Outline each uninfected red blood cell.
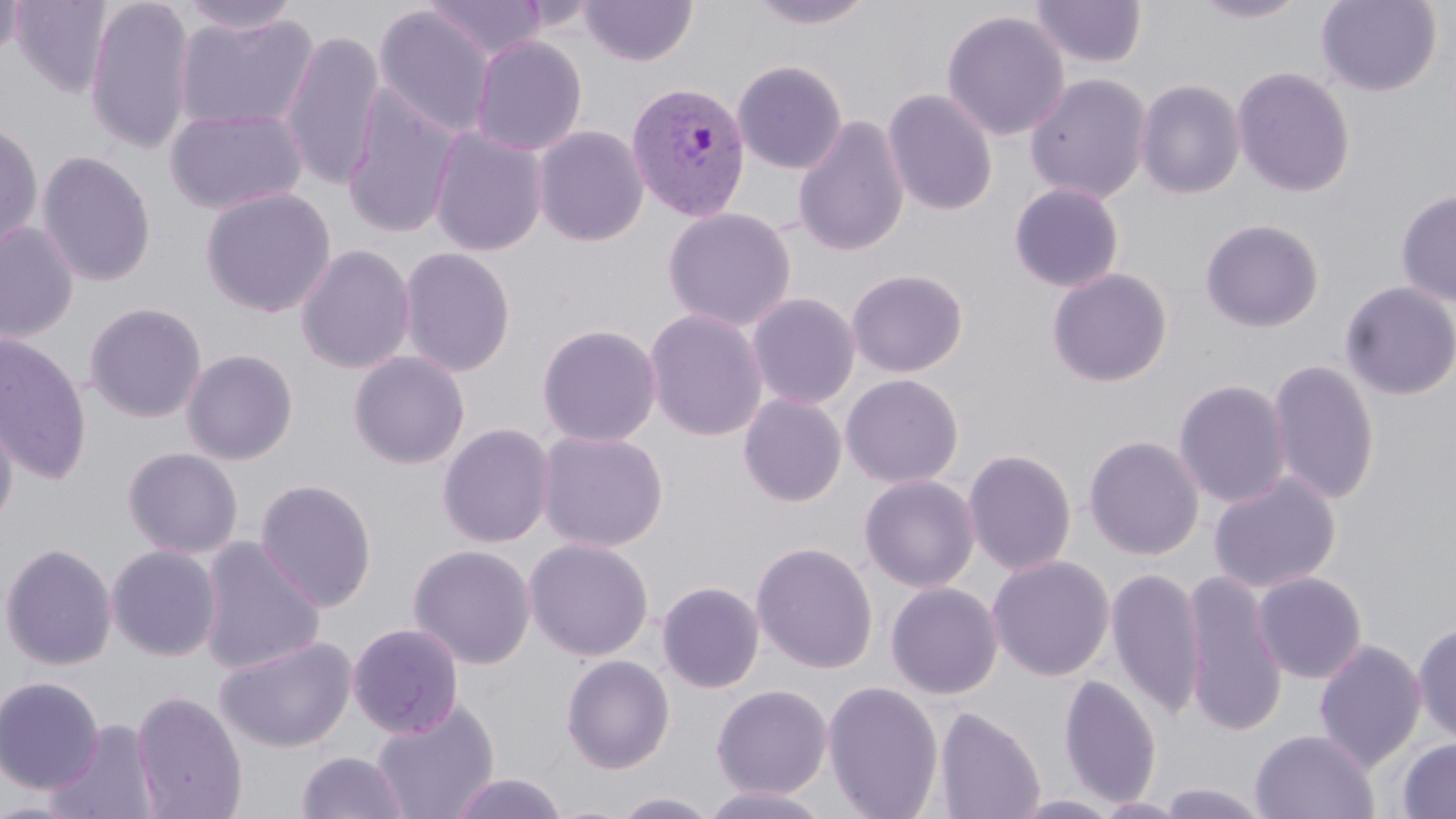

Approximate bounding boxes as (x1,y1)-(x2,y2) corner pairs in pixels.
Uninfected red blood cells: (0,0)-(25,68), (9,0)-(114,98), (83,0)-(197,156), (176,0)-(303,36), (424,0)-(548,60), (578,0)-(699,67), (744,0)-(880,30), (1191,0)-(1310,23), (1315,0)-(1442,96), (1031,1)-(1147,69), (373,5)-(497,139), (941,10)-(1070,142), (173,12)-(320,133), (279,28)-(385,192), (469,34)-(589,156), (732,59)-(848,174), (1231,67)-(1356,198), (1025,73)-(1152,204), (1135,79)-(1246,199), (342,86)-(463,239), (882,88)-(998,216), (163,107)-(308,216), (793,115)-(910,257), (0,121)-(44,254), (532,124)-(649,247), (427,125)-(549,257), (36,150)-(157,287), (1009,182)-(1125,292), (199,187)-(337,318), (1395,189)-(1456,306), (662,207)-(797,331), (1200,219)-(1324,333), (0,222)-(79,343), (294,243)-(415,374), (397,246)-(517,378), (846,268)-(968,378), (1046,268)-(1172,388), (1339,281)-(1456,401), (747,292)-(861,409), (83,302)-(207,423), (644,308)-(768,442), (536,323)-(662,447), (0,332)-(93,483), (180,348)-(299,465), (348,351)-(470,469), (1267,359)-(1380,505), (840,373)-(964,488), (1173,379)-(1291,508), (738,392)-(848,507), (0,400)-(18,532), (437,422)-(555,548), (535,429)-(669,553), (1083,435)-(1204,561), (123,447)-(243,559), (963,449)-(1077,576), (1208,472)-(1340,594), (858,474)-(980,593), (254,477)-(377,612), (550,536)-(666,772), (197,537)-(326,674), (523,537)-(654,662), (751,541)-(878,674), (0,542)-(118,671), (106,544)-(222,661), (408,544)-(536,669), (987,554)-(1115,682), (1106,567)-(1205,719), (1252,571)-(1367,684), (1180,572)-(1287,736), (657,581)-(766,693), (885,582)-(1003,699), (1412,621)-(1456,745), (347,622)-(464,739), (215,635)-(357,753), (1314,640)-(1425,771), (560,654)-(675,774), (1058,674)-(1161,808), (0,676)-(105,794), (821,679)-(944,819), (711,684)-(833,799), (132,688)-(248,819), (370,700)-(500,819), (933,705)-(1045,819), (45,718)-(161,819), (1250,729)-(1379,819), (1397,737)-(1456,818), (295,750)-(408,819), (448,772)-(570,819), (1154,782)-(1272,818), (696,785)-(836,819), (610,791)-(723,818), (1008,794)-(1125,819), (0,797)-(87,817), (1092,797)-(1195,818).

Plasmodium vivax-infected red blood cell locations: (626,81)-(752,221). Slide-level diagnosis: Plasmodium vivax. Thin blood smear. May-Grünwald-Giemsa-stained preparation. Captured at 1000x magnification. Image is 1456×819 pixels. One field of a larger specimen. Optical microscopy.